Report the malaria status of this cell.
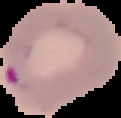
Parasitized.

image_type: cell region segmented out of the field of view; surrounding area masked to black
preparation: thin blood smear
image_size: 121×118 pixels